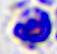

Summary:
  - Modality: photomicrograph
  - Identification: leukocyte
  - Magnification: 400x